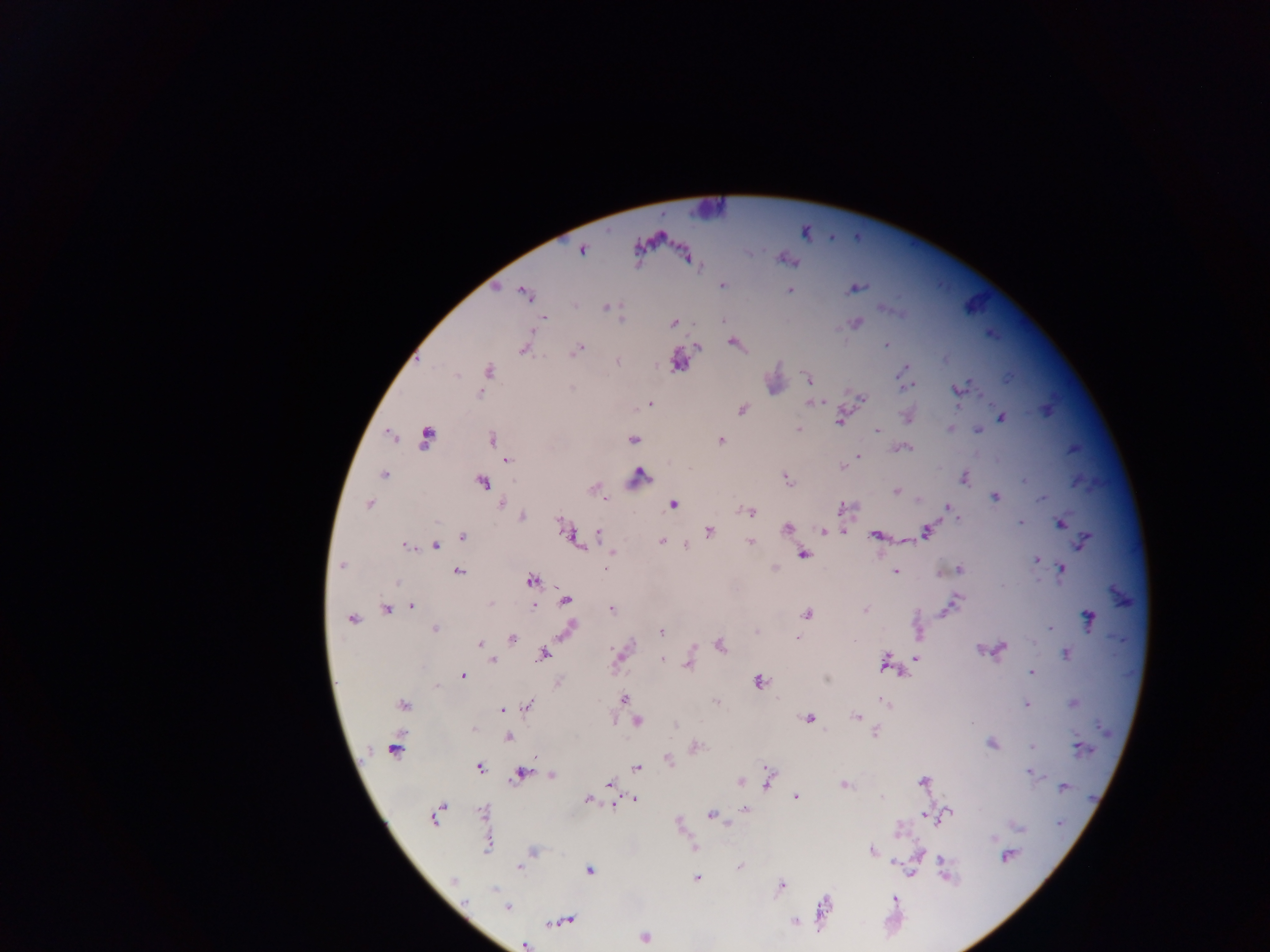

Approximate centers as {x, y} in pixels.
Summary:
  - Plasmodium parasite locations: {581, 251}, {722, 284}, {856, 288}, {790, 289}, {497, 290}, {525, 293}, {607, 308}, {889, 308}, {544, 319}, {621, 319}, {673, 322}, {856, 324}, {733, 343}, {885, 344}, {697, 347}, {524, 350}, {577, 350}, {678, 360}, {617, 361}, {487, 370}, {902, 370}, {807, 379}, {970, 382}, {911, 386}, {573, 388}, {479, 393}, {862, 399}, {650, 402}, {810, 402}, {957, 405}, {742, 408}, {1002, 417}, {840, 420}, {951, 427}, {798, 428}, {876, 430}, {979, 430}, {492, 438}, {632, 438}, {720, 439}, {906, 447}, {859, 455}, {507, 460}, {383, 473}, {785, 478}, {896, 490}, {605, 498}, {995, 498}, {1042, 498}, {367, 503}, {674, 504}, {504, 505}, {751, 513}, {955, 514}, {521, 517}, {1019, 521}, {1062, 522}, {928, 527}, {788, 528}, {845, 529}, {599, 530}, {822, 530}, {707, 532}, {875, 535}, {465, 537}, {574, 537}, {1085, 539}, {663, 540}, {750, 541}, {436, 547}, {408, 548}, {611, 551}, {803, 555}, {1037, 560}, {341, 566}, {607, 567}, {1062, 567}, {957, 570}, {895, 571}, {459, 573}, {531, 582}, {957, 599}, {565, 600}, {411, 606}, {534, 609}, {865, 609}, {386, 610}, {611, 610}, {940, 612}, {806, 613}, {1088, 617}, {353, 619}, {571, 625}, {1049, 628}, {434, 630}, {661, 632}, {798, 637}, {512, 639}, {481, 643}, {720, 644}, {1004, 647}, {979, 650}, {543, 655}, {618, 657}, {917, 658}, {672, 659}, {492, 661}, {688, 664}, {1031, 673}, {903, 674}, {464, 676}, {827, 678}, {759, 681}, {437, 687}, {623, 700}, {1026, 704}, {404, 705}, {520, 709}, {501, 710}, {858, 717}, {809, 719}, {638, 721}, {875, 731}, {509, 737}, {991, 742}, {1077, 744}, {1031, 748}, {481, 767}, {638, 767}, {1029, 772}, {521, 773}, {551, 774}, {922, 781}, {610, 782}, {742, 782}, {767, 782}, {845, 784}, {1064, 787}, {797, 797}, {587, 799}, {635, 799}, {613, 804}, {745, 809}, {950, 813}, {435, 814}, {925, 814}, {710, 815}, {1057, 825}, {1021, 828}, {872, 851}, {1008, 856}, {942, 860}, {893, 861}, {519, 868}, {591, 870}, {912, 871}, {696, 878}, {452, 881}, {781, 886}, {495, 890}, {464, 902}, {507, 908}, {825, 908}, {563, 922}, {645, 937}, {527, 944}
  - Field of view: single
  - Capture: mobile-phone photograph through a microscope
  - Preparation: thick blood smear
  - Country: Ghana
  - Image size: 1270×952 pixels